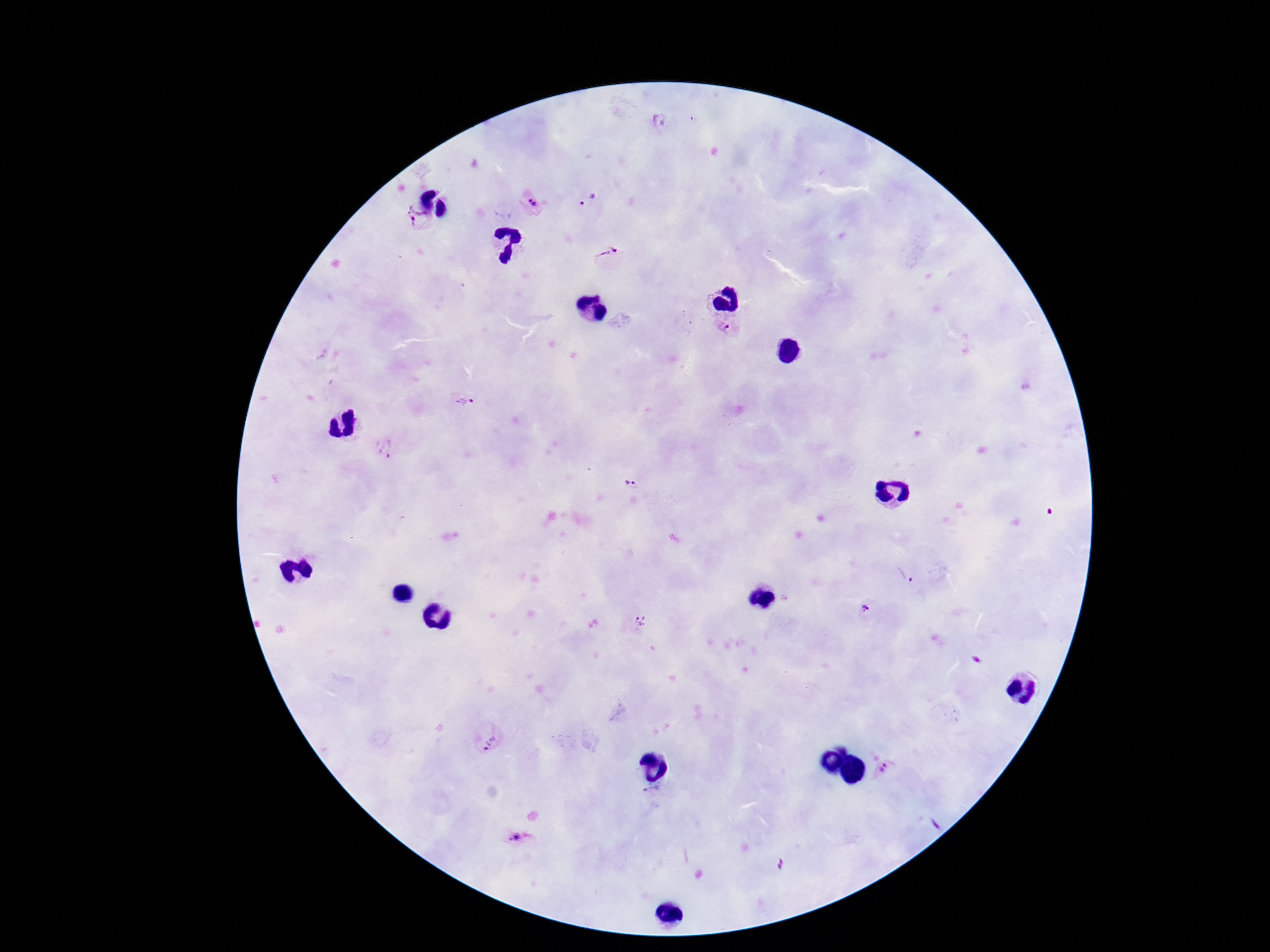
image size = 1270×952 pixels
preparation = thick blood smear
field of view = single
patient malaria status = infected
stain = Giemsa
magnification = 100x
Plasmodium parasite locations = approximate centers as {x, y} in pixels: {589, 201}, {533, 203}, {415, 216}, {609, 256}, {728, 330}, {464, 402}, {385, 447}, {631, 485}, {905, 576}, {864, 609}, {640, 620}, {491, 743}, {884, 769}, {652, 795}, {516, 836}
capture = smartphone camera through the microscope eyepiece